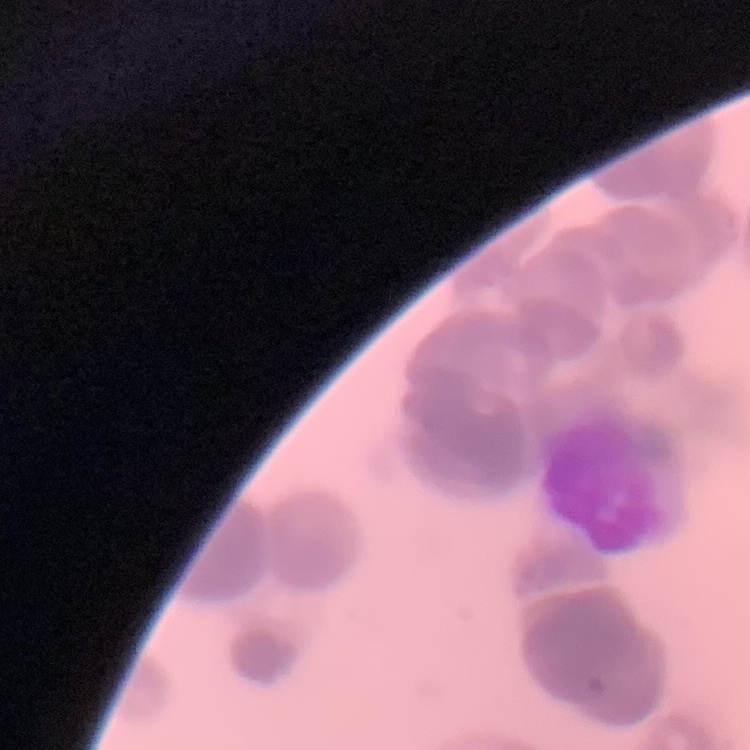
red blood cell morphology = rouleaux formation
stain = Field's or Giemsa
image type = one tile cut from a larger photomicrograph
preparation = thin peripheral smear